Classify this cell by malaria status.
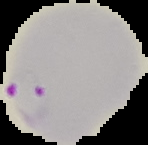

Parasitized.

{
  "preparation": "thin blood smear",
  "image_type": "segmented cell region on a black background",
  "image_size": "148×145 pixels"
}